Locate and identify every blood parasite.
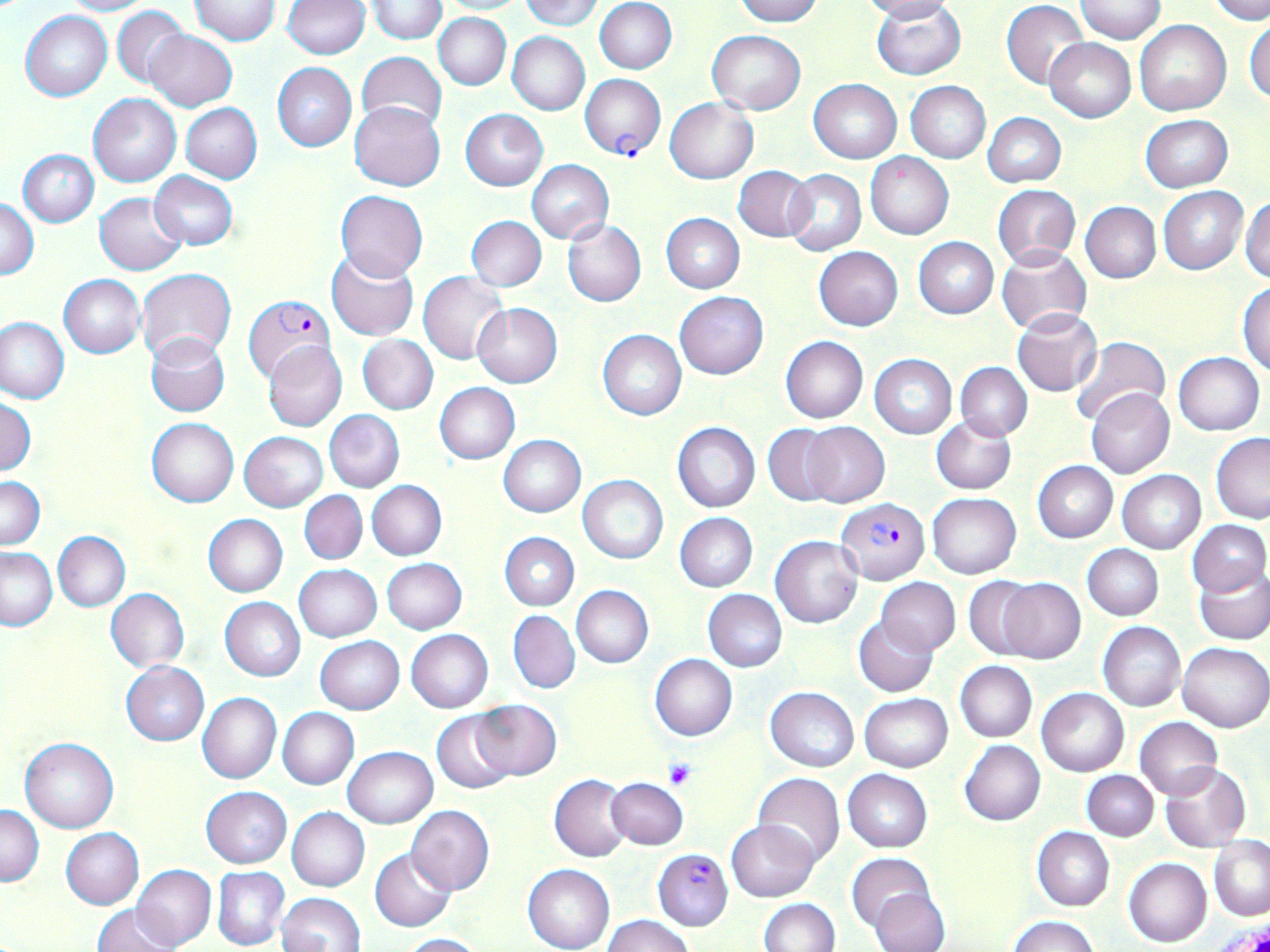
Approximate bounding boxes as (x1, y1, x2, y2) in pixels.
Plasmodium falciparum-infected red blood cells: (580, 73, 666, 159), (243, 295, 336, 382), (836, 498, 931, 584), (652, 847, 733, 930).
No Plasmodium ovale, Plasmodium malariae, Plasmodium vivax, Babesia divergens, or Trypanosoma brucei observed.

slide_level_diagnosis: Plasmodium falciparum
magnification: 1000x
modality: light microscopy
preparation: thin blood smear
field_of_view: one of a larger specimen
image_size: 1270×952 pixels
platelet_locations: 'approximate bounding boxes as (x1, y1, x2, y2) in pixels: (663, 758, 697, 790)'
uninfected_red_blood_cell_locations: 'approximate bounding boxes as (x1, y1, x2, y2) in pixels: (57, 0, 152, 16), (282, 0, 369, 59), (435, 0, 528, 14), (520, 0, 603, 30), (595, 0, 676, 74), (735, 0, 821, 26), (863, 0, 957, 22), (1002, 0, 1088, 90), (1077, 0, 1166, 43), (1209, 0, 1270, 23), (189, 1, 280, 46), (367, 2, 445, 43), (872, 2, 965, 80), (111, 5, 188, 89), (21, 11, 111, 101), (433, 13, 511, 90), (1245, 14, 1270, 104), (1135, 21, 1230, 116), (146, 30, 237, 111), (707, 30, 805, 113), (507, 31, 590, 115), (1044, 38, 1136, 123), (356, 52, 447, 135), (272, 62, 356, 151), (808, 79, 901, 163), (906, 81, 990, 163), (89, 93, 182, 187), (665, 97, 758, 184), (350, 102, 446, 191), (180, 103, 262, 183), (461, 109, 548, 191), (983, 113, 1066, 187), (1140, 115, 1232, 192), (18, 148, 98, 226), (865, 152, 953, 239), (526, 160, 614, 244), (733, 165, 817, 243), (783, 169, 866, 256), (148, 171, 238, 250), (993, 184, 1080, 268), (1158, 185, 1249, 274), (337, 190, 427, 280), (95, 192, 186, 275), (1241, 194, 1269, 283), (1, 196, 39, 281), (1081, 202, 1161, 283), (662, 213, 744, 292), (466, 216, 546, 291), (562, 220, 647, 306), (914, 237, 998, 318), (997, 245, 1091, 335), (814, 246, 903, 331), (326, 249, 418, 341), (138, 268, 236, 363), (418, 272, 508, 363), (59, 274, 146, 358), (1238, 281, 1270, 375), (675, 291, 768, 378), (473, 303, 561, 387), (1013, 308, 1103, 397), (1, 316, 69, 404), (597, 330, 686, 420), (146, 334, 230, 416), (359, 335, 438, 414), (780, 335, 868, 423), (1072, 337, 1171, 426), (262, 340, 346, 432), (1173, 352, 1265, 435), (869, 354, 957, 439), (956, 362, 1032, 440), (435, 383, 520, 464), (1087, 388, 1174, 478), (1, 396, 35, 476), (323, 409, 404, 492), (932, 417, 1016, 494), (147, 418, 239, 507), (673, 422, 760, 512), (801, 422, 889, 508), (763, 423, 842, 505), (239, 431, 327, 511), (498, 434, 586, 516), (1211, 435, 1270, 524), (1032, 461, 1118, 543), (1118, 470, 1206, 554), (578, 475, 668, 564), (0, 477, 45, 549), (367, 480, 446, 559), (299, 491, 367, 565), (927, 493, 1020, 579), (675, 513, 759, 592), (202, 514, 288, 598), (1187, 519, 1268, 598), (52, 530, 130, 612), (500, 532, 579, 610), (770, 535, 863, 629), (1082, 544, 1164, 621), (1, 548, 57, 630), (382, 558, 467, 634), (294, 564, 381, 641), (1196, 570, 1270, 645), (964, 576, 1048, 660), (877, 578, 960, 655), (998, 578, 1086, 662), (571, 585, 653, 668), (106, 589, 190, 672), (702, 589, 787, 671), (220, 597, 306, 681), (508, 611, 580, 694), (853, 617, 938, 697), (1098, 622, 1185, 712), (405, 629, 493, 713), (315, 636, 404, 714), (1178, 643, 1270, 732), (650, 654, 738, 741), (955, 660, 1036, 743), (120, 661, 208, 746), (765, 687, 859, 771), (1036, 688, 1128, 777), (198, 692, 282, 784), (860, 693, 952, 771), (471, 699, 561, 780), (277, 707, 359, 789), (433, 712, 516, 794), (1134, 717, 1223, 799), (21, 738, 118, 832), (960, 740, 1045, 825), (343, 746, 437, 828), (1160, 762, 1250, 853), (843, 769, 933, 852), (1082, 770, 1159, 842), (753, 773, 844, 865), (550, 774, 632, 861), (606, 778, 687, 850), (201, 787, 292, 869), (407, 805, 494, 894), (1, 806, 45, 886), (287, 808, 369, 891), (727, 819, 820, 902), (60, 827, 143, 909), (1032, 827, 1115, 911), (1209, 837, 1270, 921), (370, 848, 455, 931), (847, 852, 937, 933), (1124, 857, 1212, 948), (523, 864, 615, 952), (131, 865, 216, 949), (212, 866, 290, 950), (871, 890, 949, 952), (277, 893, 365, 951), (758, 898, 840, 951), (92, 904, 178, 952), (601, 914, 695, 952), (1008, 915, 1100, 952), (400, 932, 484, 951)'
stain: May-Grünwald-Giemsa